Locate every Plasmodium falciparum parasite and identify its life-cycle stage.
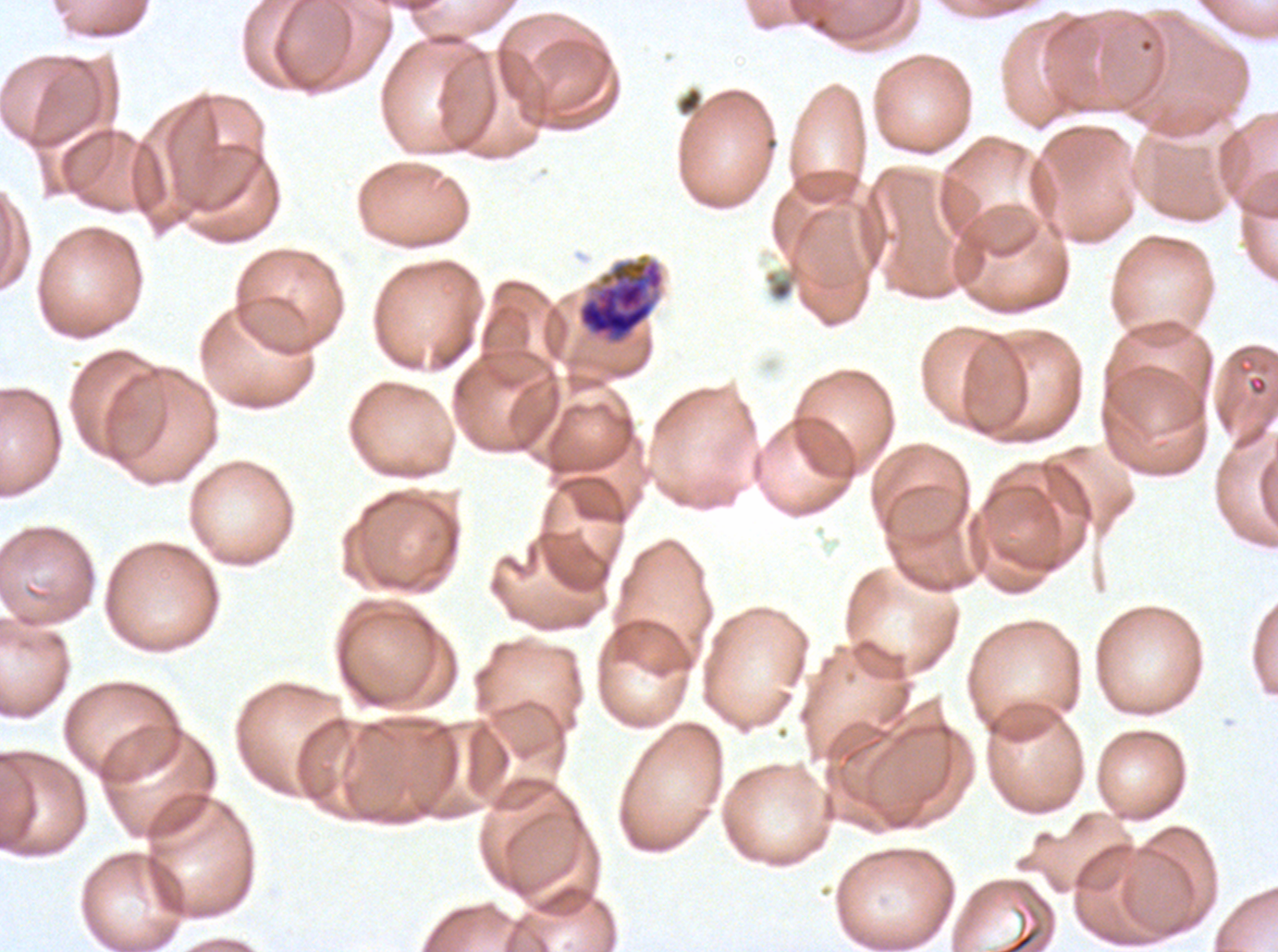

Approximate bounding boxes as [x1, y1, x2, y2] in pixels.
Late schizonts: [576, 258, 665, 346].
No rings, late-ring/early-trophozoite forms, mid trophozoites, late trophozoites, early schizonts, segmenters, or gametocytes observed.

debris locations = [676, 86, 704, 117], [765, 271, 794, 301]
specimen = Plasmodium falciparum cultured ex vivo for 24 to 48 hours, from a patient in The Gambia
image size = 1278×952 pixels
stain = Giemsa
preparation = thin blood film
field of view = sub-image separated from a larger composite